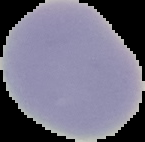
From a thin blood smear. Image is 145×142 pixels. The area outside the segmented cell region is set to black. Result: no malaria parasites detected.